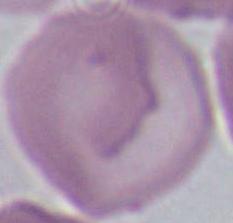
identification: erythrocyte
magnification: 1000x
modality: micrograph